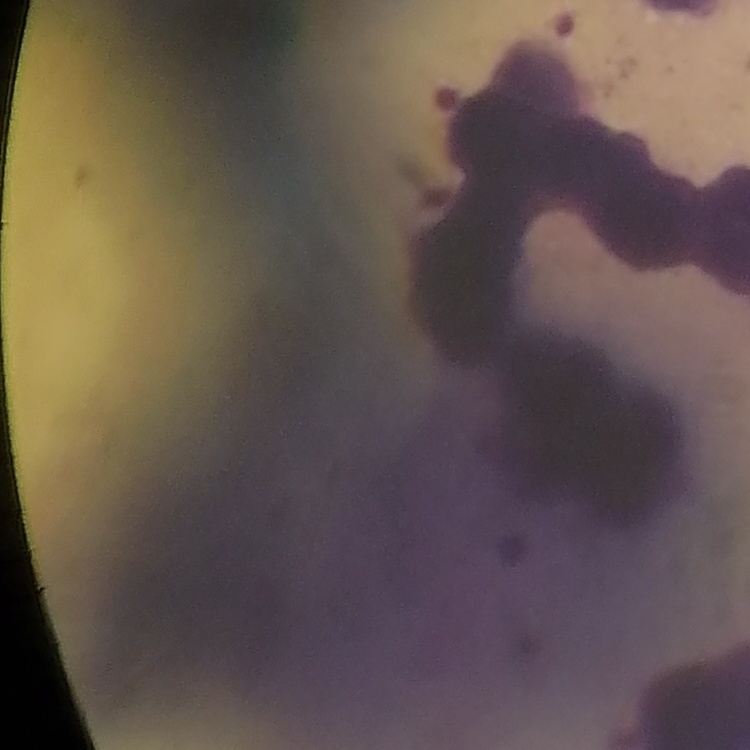
erythrocyte_morphology: rouleaux formation
preparation: thin peripheral smear
stain: Field's or Giemsa
image_type: square crop of a larger photomicrograph